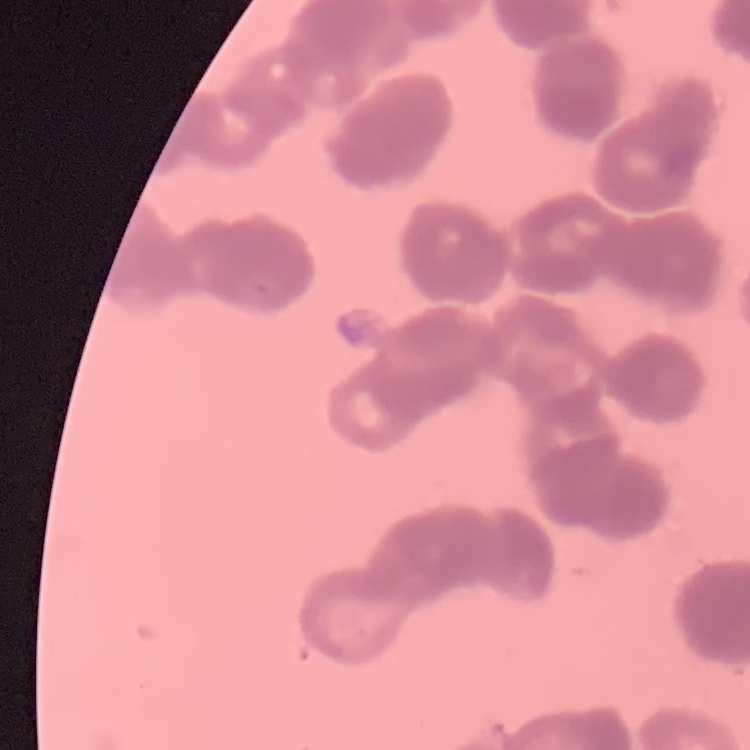
The red blood cells show rouleaux formation. Thin peripheral smear. Square crop of a larger photomicrograph. Field's or Giemsa stain.